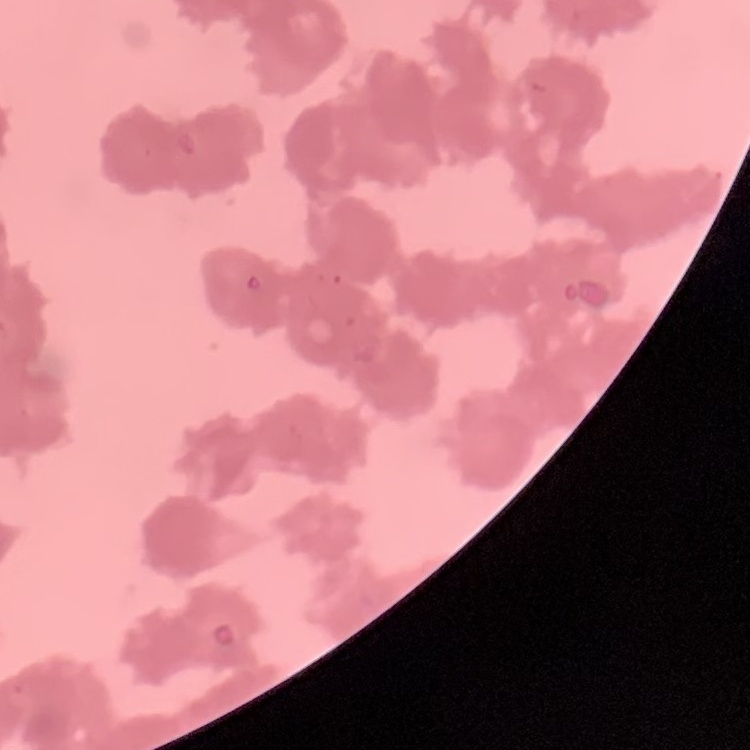

The erythrocytes show rouleaux formation. Thin peripheral smear. Square crop of a larger photomicrograph. Stained with either Field's or Giemsa.